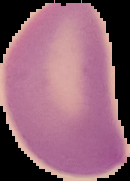
The area outside the segmented cell region is set to black. From a thin blood smear. Image is 130×181 pixels. Result: no Plasmodium parasites detected.